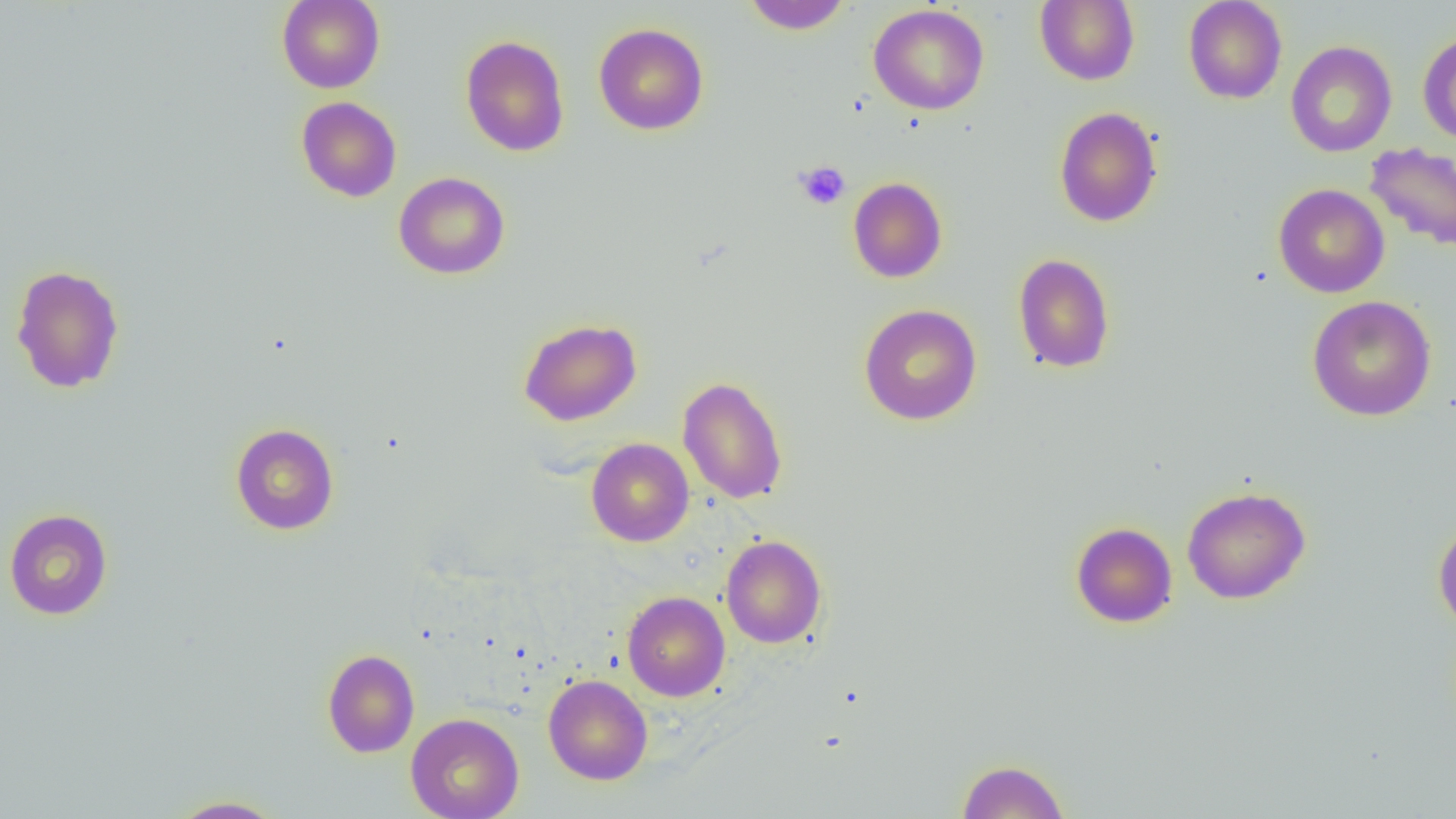

Approximate bounding boxes as named x1/y1/x2/y2 corners in pixels. Platelet locations: (x1=794, y1=161, x2=850, y2=209). Uninfected red blood cell locations: (x1=277, y1=0, x2=385, y2=93), (x1=741, y1=0, x2=853, y2=34), (x1=1035, y1=0, x2=1140, y2=86), (x1=1183, y1=0, x2=1288, y2=104), (x1=868, y1=4, x2=989, y2=115), (x1=594, y1=22, x2=709, y2=135), (x1=1417, y1=30, x2=1456, y2=145), (x1=460, y1=35, x2=570, y2=157), (x1=1285, y1=41, x2=1397, y2=157), (x1=296, y1=96, x2=402, y2=202), (x1=1054, y1=106, x2=1163, y2=227), (x1=1365, y1=142, x2=1456, y2=252), (x1=393, y1=172, x2=510, y2=279), (x1=848, y1=177, x2=947, y2=283), (x1=1273, y1=183, x2=1390, y2=298), (x1=1012, y1=253, x2=1115, y2=373), (x1=10, y1=263, x2=125, y2=394), (x1=1307, y1=295, x2=1437, y2=421), (x1=858, y1=304, x2=982, y2=425), (x1=518, y1=318, x2=642, y2=425), (x1=678, y1=376, x2=788, y2=504), (x1=230, y1=423, x2=340, y2=535), (x1=586, y1=438, x2=694, y2=546), (x1=1181, y1=486, x2=1311, y2=605), (x1=3, y1=508, x2=113, y2=620), (x1=1433, y1=518, x2=1456, y2=633), (x1=1070, y1=522, x2=1178, y2=628), (x1=720, y1=535, x2=828, y2=648), (x1=622, y1=591, x2=730, y2=701), (x1=321, y1=649, x2=420, y2=758), (x1=543, y1=675, x2=653, y2=784), (x1=406, y1=713, x2=524, y2=819), (x1=957, y1=758, x2=1069, y2=818), (x1=166, y1=795, x2=286, y2=818). Slide-level diagnosis: negative for blood parasites. Thin blood smear. 1000x magnification. Image is 1456×819 pixels. Optical microscopy. Single field of view.